Locate every blood parasite and identify its species.
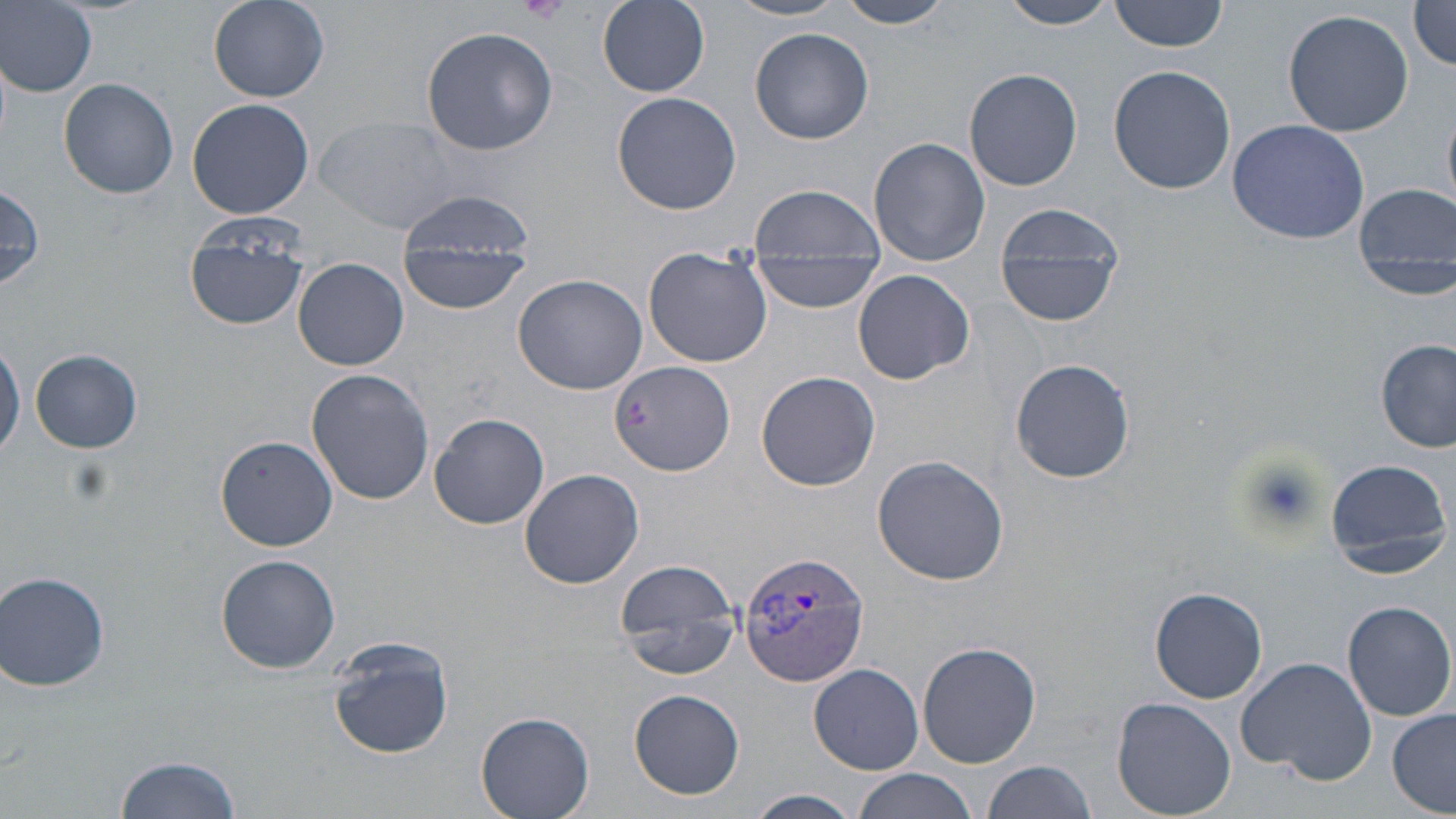

Approximate bounding boxes as (x1, y1, x2, y2) in pixels.
Plasmodium vivax-infected red blood cells: (738, 549, 871, 688).
No Plasmodium falciparum, Plasmodium ovale, Plasmodium malariae, Babesia divergens, or Trypanosoma brucei observed.

slide-level diagnosis = Plasmodium vivax
image size = 1456×819 pixels
platelet locations = approximate bounding boxes as (x1, y1, x2, y2) in pixels: (515, 0, 572, 24), (1239, 453, 1328, 532)
magnification = 1000x
preparation = thin blood smear
stain = May-Grünwald-Giemsa
uninfected red blood cell locations = approximate bounding boxes as (x1, y1, x2, y2) in pixels: (207, 0, 330, 102), (836, 0, 958, 28), (1000, 0, 1123, 30), (1109, 0, 1232, 53), (1409, 0, 1456, 74), (3, 1, 98, 95), (728, 1, 848, 22), (597, 2, 711, 97), (1282, 8, 1416, 138), (422, 26, 557, 156), (749, 27, 874, 144), (1108, 64, 1236, 195), (964, 67, 1083, 191), (60, 79, 179, 200), (611, 92, 742, 214), (186, 97, 315, 220), (317, 114, 470, 235), (1227, 117, 1372, 245), (869, 137, 990, 267), (0, 183, 46, 293), (1352, 183, 1456, 300), (749, 185, 886, 259), (992, 200, 1128, 329), (184, 216, 311, 333), (398, 217, 533, 314), (642, 248, 772, 368), (747, 255, 883, 311), (295, 257, 408, 370), (853, 269, 975, 384), (511, 273, 647, 394), (0, 333, 24, 463), (1376, 339, 1455, 452), (30, 349, 144, 454), (1010, 357, 1136, 484), (609, 361, 735, 477), (306, 369, 436, 505), (756, 370, 881, 491), (427, 411, 548, 531), (217, 435, 337, 551), (872, 454, 1008, 586), (1321, 457, 1453, 578), (519, 467, 645, 590), (216, 553, 341, 675), (614, 558, 742, 679), (1, 570, 111, 692), (1149, 586, 1269, 703), (1342, 600, 1455, 720), (326, 637, 455, 762), (917, 640, 1042, 769), (1236, 656, 1377, 781), (809, 663, 924, 774), (629, 688, 745, 800), (1112, 698, 1237, 819), (1387, 709, 1455, 816), (477, 710, 596, 818), (114, 753, 245, 819), (980, 760, 1097, 819), (852, 769, 978, 819), (745, 790, 863, 819)
field of view = single
modality = optical microscopy